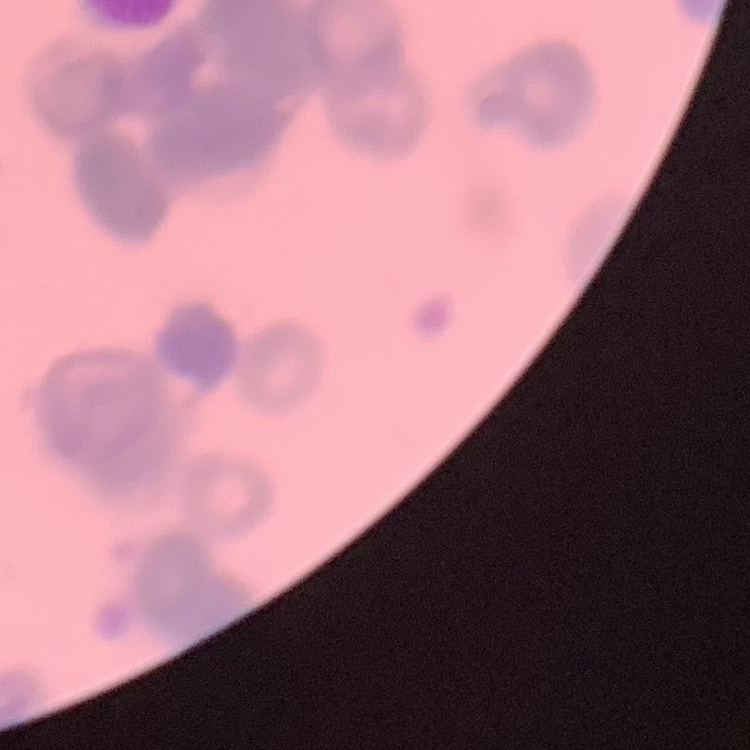

{
  "erythrocyte_morphology": "rouleaux formation",
  "stain": "Field's or Giemsa",
  "image_type": "one tile cut from a larger photomicrograph",
  "preparation": "thin blood smear"
}